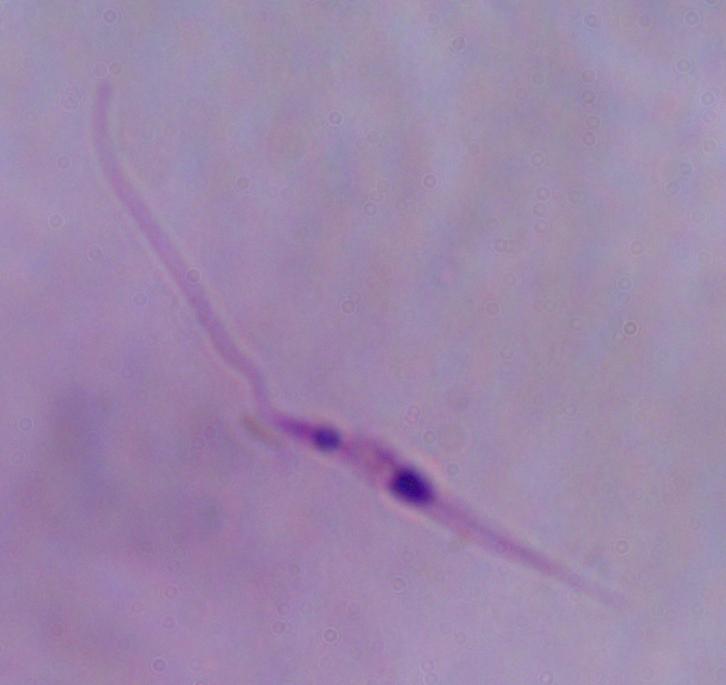

Summary:
  - Magnification: 1000x
  - Modality: photomicrograph
  - Identification: Leishmania